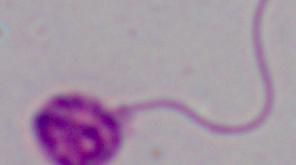 A Leishmania parasite is shown. Captured at 1000x magnification. Micrograph.